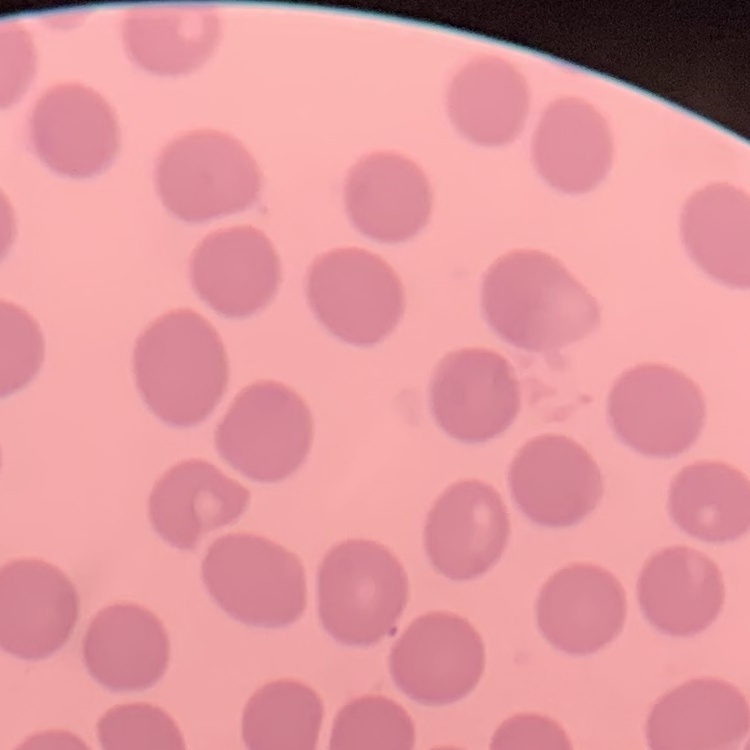

The red blood cells show no rouleaux formation. Square crop of a larger photomicrograph. Thin blood smear. Field's or Giemsa stain.